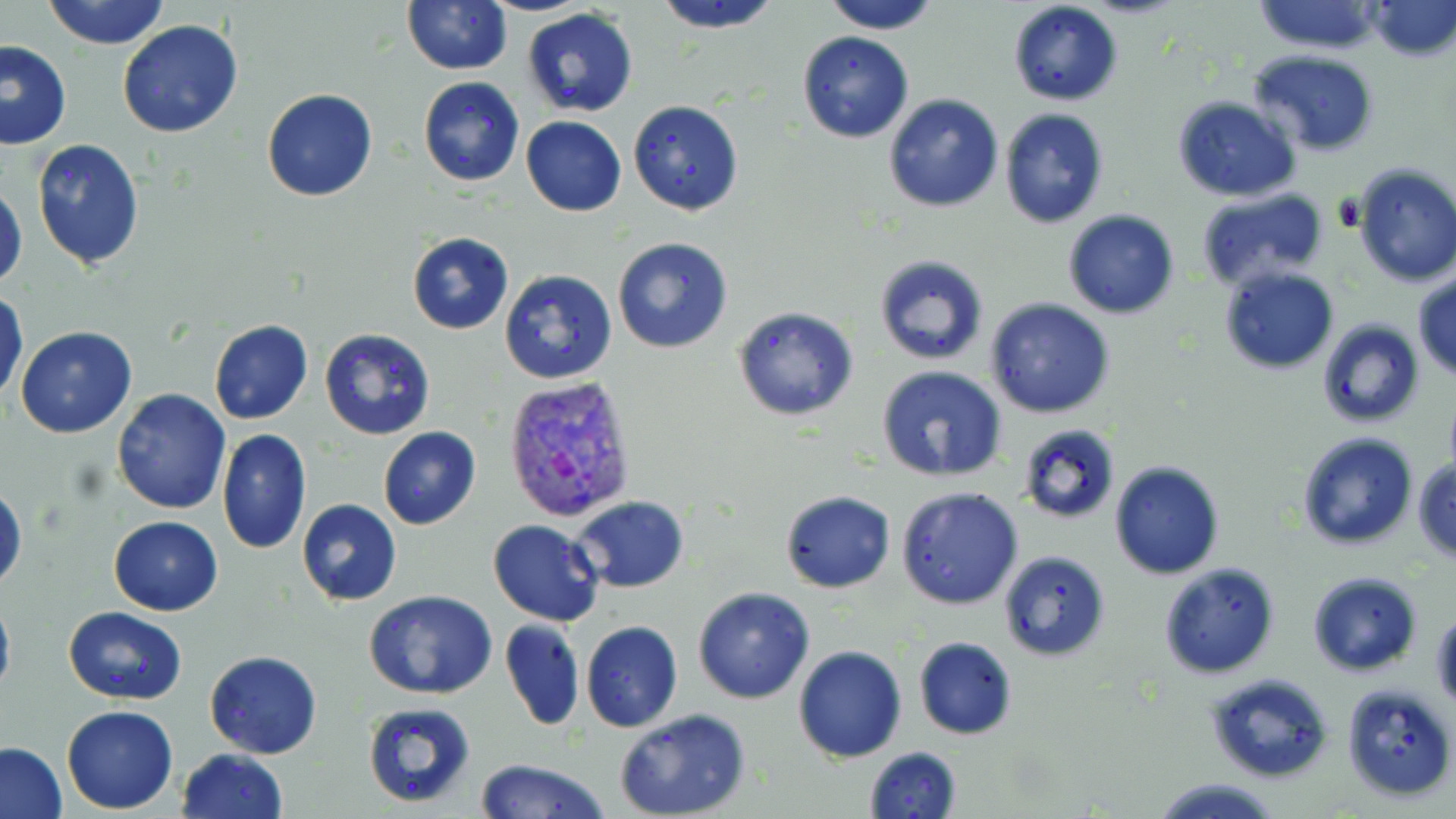
Summary:
  - Coordinate format: approximate bounding boxes as [x1, y1, x2, y2] in pixels
  - Uninfected red blood cell locations: [42, 0, 171, 49], [402, 0, 512, 74], [651, 0, 786, 34], [817, 0, 945, 34], [1249, 0, 1386, 55], [1007, 1, 1124, 107], [1367, 1, 1456, 61], [519, 9, 639, 117], [115, 20, 243, 139], [797, 30, 915, 143], [0, 40, 72, 151], [1247, 49, 1380, 156], [418, 77, 525, 187], [261, 88, 378, 202], [883, 92, 1004, 213], [1171, 96, 1299, 202], [628, 101, 744, 217], [999, 108, 1109, 228], [520, 115, 627, 217], [31, 139, 145, 270], [1350, 163, 1456, 288], [0, 182, 27, 293], [1195, 186, 1329, 290], [1063, 210, 1180, 320], [406, 231, 513, 335], [612, 237, 735, 355], [874, 254, 990, 368], [1219, 268, 1340, 375], [498, 269, 618, 385], [1412, 271, 1456, 380], [0, 289, 28, 405], [985, 298, 1115, 420], [732, 305, 858, 422], [209, 319, 313, 425], [1317, 319, 1424, 428], [16, 326, 137, 439], [319, 328, 435, 441], [876, 367, 1008, 484], [112, 388, 230, 514], [1018, 423, 1120, 523], [377, 427, 480, 531], [217, 429, 311, 553], [1296, 432, 1419, 551], [1412, 458, 1456, 564], [1108, 459, 1225, 578], [0, 485, 25, 591], [896, 486, 1022, 611], [780, 490, 895, 594], [572, 496, 690, 592], [297, 499, 402, 606], [108, 516, 223, 615], [488, 518, 605, 627], [997, 549, 1111, 662], [1158, 561, 1282, 679], [1306, 570, 1425, 676], [694, 587, 815, 704], [0, 588, 15, 704], [364, 591, 497, 698], [63, 606, 187, 704], [1432, 609, 1456, 714], [500, 618, 584, 731], [581, 621, 683, 732], [912, 636, 1019, 740], [792, 645, 908, 764], [204, 650, 323, 759], [1203, 672, 1334, 784], [1341, 682, 1456, 806], [362, 702, 477, 809], [62, 705, 179, 813], [613, 710, 751, 819], [0, 743, 68, 818], [862, 746, 963, 819], [175, 748, 289, 819], [472, 759, 612, 819], [1149, 776, 1284, 818]
  - Plasmodium vivax-infected red blood cell locations: [502, 378, 639, 522]
  - Slide-level diagnosis: Plasmodium vivax
  - Modality: light microscopy
  - Stain: May-Grünwald-Giemsa
  - Field of view: single
  - Magnification: 1000x
  - Preparation: thin blood film
  - Image size: 1456×819 pixels